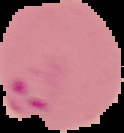

Summary:
  - Image type: cell region segmented out of the field of view; surrounding area masked to black
  - Image size: 124×133 pixels
  - Preparation: thin blood film
  - Result: Plasmodium parasites detected